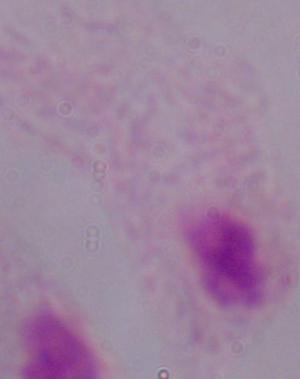
Summary:
  - Modality: photomicrograph
  - Magnification: 1000x
  - Identification: trichomonad